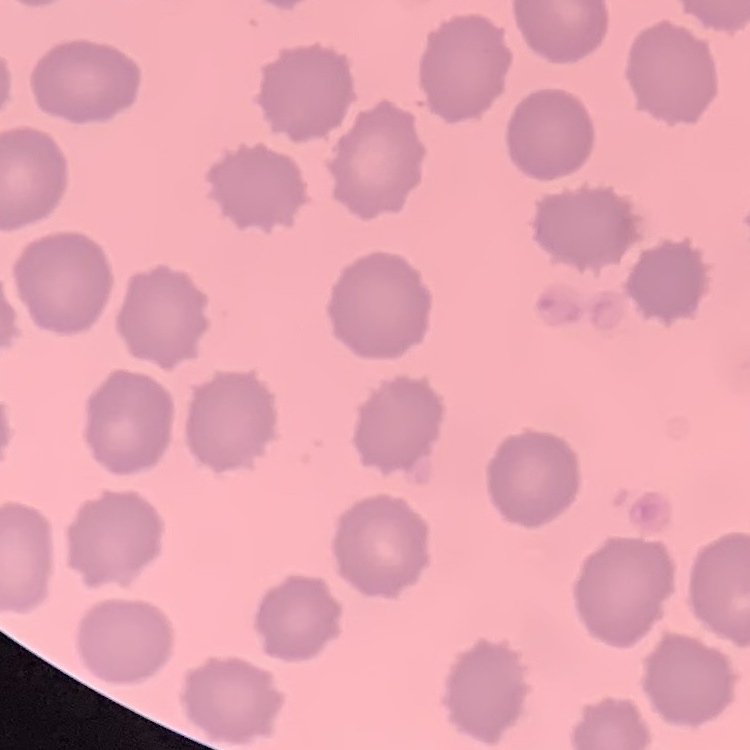
Summary:
  - Erythrocyte morphology: no rouleaux formation
  - Preparation: thin blood smear
  - Stain: Field's or Giemsa
  - Image type: square crop of a larger photomicrograph